Identify the blood parasite species.
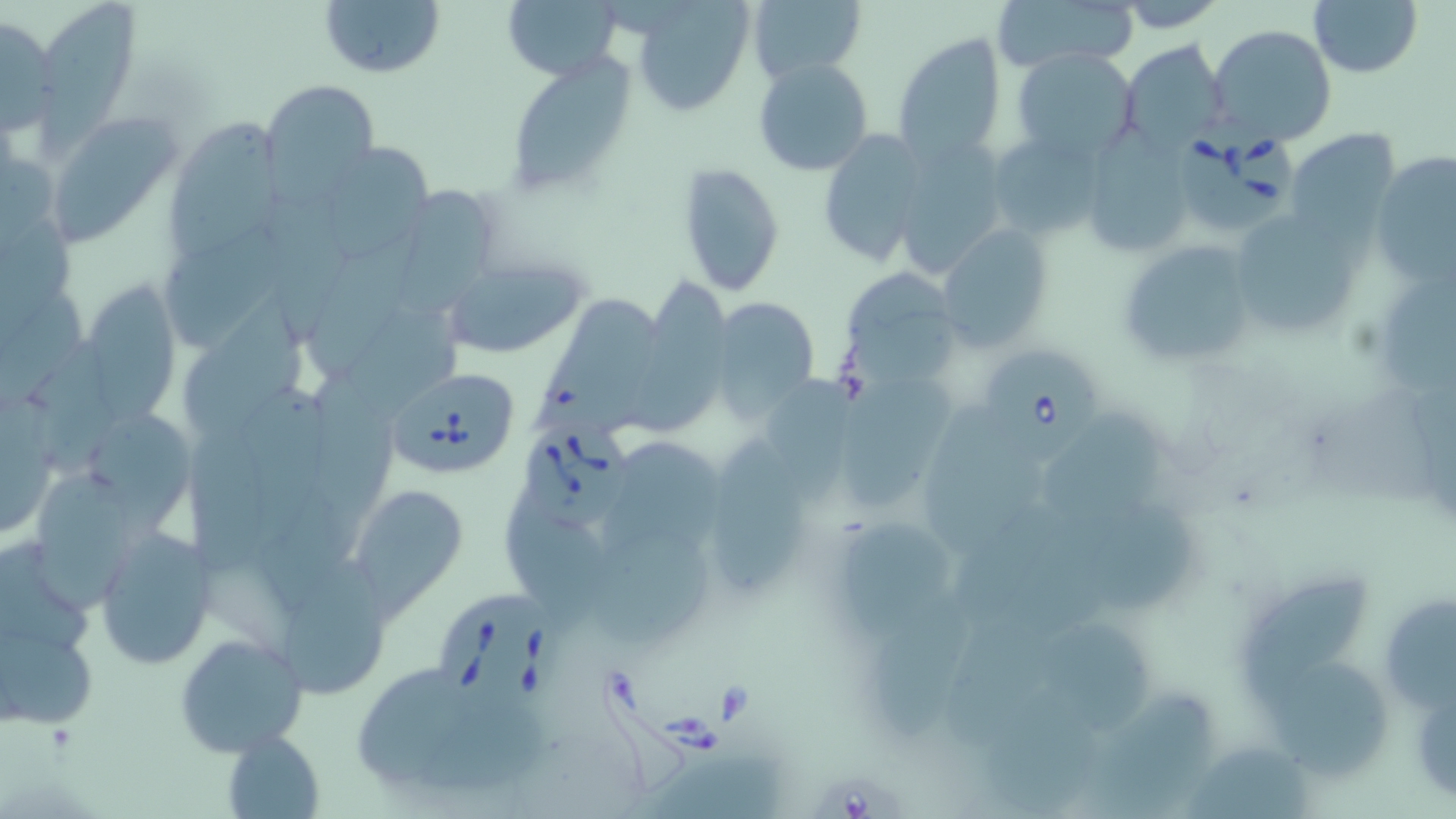
Babesia divergens.

Summary:
  - Coordinate format: approximate bounding boxes as named x1/y1/x2/y2 corners in pixels
  - Uninfected red blood cell locations: (x1=319, y1=0, x2=444, y2=78), (x1=503, y1=0, x2=625, y2=81), (x1=632, y1=0, x2=753, y2=115), (x1=751, y1=0, x2=866, y2=80), (x1=997, y1=0, x2=1135, y2=72), (x1=1308, y1=0, x2=1423, y2=77), (x1=39, y1=1, x2=144, y2=164), (x1=1113, y1=1, x2=1229, y2=32), (x1=0, y1=14, x2=58, y2=135), (x1=1208, y1=26, x2=1337, y2=147), (x1=893, y1=32, x2=1008, y2=164), (x1=1121, y1=40, x2=1229, y2=156), (x1=1013, y1=49, x2=1141, y2=164), (x1=753, y1=57, x2=873, y2=175), (x1=507, y1=59, x2=635, y2=198), (x1=261, y1=79, x2=378, y2=196), (x1=47, y1=115, x2=180, y2=242), (x1=167, y1=117, x2=289, y2=256), (x1=1091, y1=120, x2=1200, y2=258), (x1=1286, y1=128, x2=1400, y2=235), (x1=815, y1=129, x2=931, y2=265), (x1=995, y1=137, x2=1108, y2=245), (x1=902, y1=141, x2=1013, y2=277), (x1=316, y1=152, x2=431, y2=256), (x1=1373, y1=152, x2=1456, y2=283), (x1=679, y1=161, x2=785, y2=297), (x1=401, y1=180, x2=501, y2=318), (x1=266, y1=191, x2=354, y2=336), (x1=1242, y1=219, x2=1365, y2=341), (x1=937, y1=226, x2=1052, y2=346), (x1=169, y1=229, x2=281, y2=348), (x1=309, y1=229, x2=434, y2=372), (x1=1115, y1=238, x2=1259, y2=369), (x1=442, y1=257, x2=590, y2=358), (x1=1377, y1=266, x2=1456, y2=399), (x1=841, y1=269, x2=963, y2=386), (x1=631, y1=275, x2=730, y2=434), (x1=82, y1=280, x2=182, y2=418), (x1=531, y1=285, x2=661, y2=438), (x1=180, y1=292, x2=319, y2=433), (x1=710, y1=295, x2=820, y2=417), (x1=48, y1=342, x2=127, y2=475), (x1=840, y1=373, x2=963, y2=509), (x1=310, y1=379, x2=410, y2=513), (x1=242, y1=384, x2=340, y2=534), (x1=919, y1=397, x2=1048, y2=553), (x1=1049, y1=411, x2=1173, y2=519), (x1=97, y1=416, x2=197, y2=534), (x1=699, y1=425, x2=815, y2=595), (x1=190, y1=427, x2=272, y2=575), (x1=609, y1=439, x2=730, y2=556), (x1=34, y1=468, x2=129, y2=610), (x1=350, y1=482, x2=469, y2=609), (x1=259, y1=486, x2=359, y2=615), (x1=1078, y1=497, x2=1201, y2=614), (x1=843, y1=515, x2=955, y2=641), (x1=591, y1=524, x2=715, y2=655), (x1=93, y1=528, x2=213, y2=668), (x1=284, y1=552, x2=390, y2=698), (x1=1236, y1=569, x2=1369, y2=710), (x1=1389, y1=592, x2=1456, y2=723), (x1=859, y1=603, x2=974, y2=739), (x1=0, y1=607, x2=100, y2=734), (x1=1039, y1=615, x2=1167, y2=739), (x1=175, y1=630, x2=309, y2=759), (x1=1274, y1=658, x2=1402, y2=776), (x1=350, y1=659, x2=531, y2=806), (x1=1093, y1=687, x2=1215, y2=819), (x1=985, y1=689, x2=1096, y2=814), (x1=222, y1=730, x2=324, y2=817), (x1=1190, y1=744, x2=1311, y2=819), (x1=649, y1=750, x2=784, y2=819)
  - Babesia divergens-infected red blood cell locations: (x1=1178, y1=117, x2=1295, y2=238), (x1=984, y1=351, x2=1102, y2=467), (x1=391, y1=368, x2=519, y2=473), (x1=526, y1=425, x2=644, y2=532), (x1=444, y1=591, x2=575, y2=718)
  - Preparation: thin blood film
  - Field of view: one of a larger specimen
  - Stain: May-Grünwald-Giemsa
  - Magnification: 1000x
  - Modality: optical microscopy
  - Image size: 1456×819 pixels